Classify this cell by malaria status.
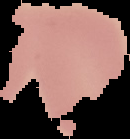

Parasitized.

Summary:
  - Preparation: thin blood smear
  - Image size: 130×139 pixels
  - Image type: segmented cell region on a black background